Outline each Plasmodium malariae-infected red blood cell.
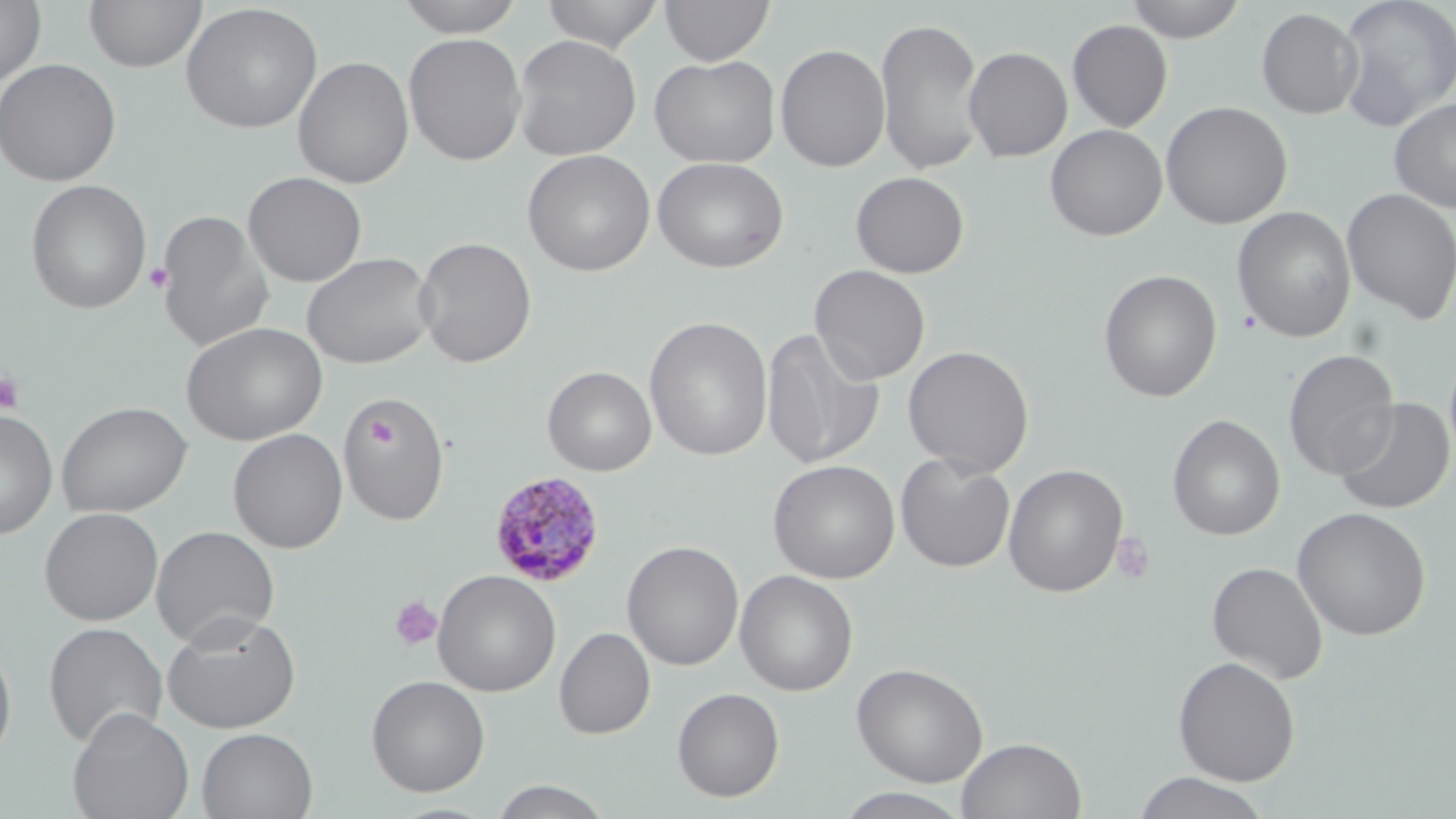

Approximate bounding boxes as (x1, y1, x2, y2) in pixels.
Plasmodium malariae-infected red blood cells: (488, 471, 606, 587).

Summary:
  - Uninfected red blood cell locations: (84, 0, 207, 73), (392, 0, 528, 37), (540, 0, 665, 51), (660, 0, 774, 65), (1125, 0, 1248, 42), (1336, 0, 1456, 131), (0, 1, 47, 88), (180, 3, 323, 133), (1256, 8, 1363, 119), (875, 15, 986, 176), (1067, 20, 1172, 132), (403, 32, 527, 166), (512, 34, 641, 160), (775, 44, 891, 171), (964, 46, 1072, 162), (649, 54, 781, 169), (292, 55, 414, 188), (0, 58, 122, 187), (1389, 98, 1456, 213), (1160, 101, 1293, 229), (1045, 124, 1167, 241), (521, 149, 656, 276), (653, 156, 789, 273), (243, 171, 367, 286), (851, 171, 969, 278), (25, 179, 151, 315), (1341, 188, 1456, 324), (1231, 206, 1357, 343), (154, 209, 274, 352), (414, 236, 537, 367), (302, 252, 436, 369), (809, 264, 931, 384), (1098, 269, 1222, 402), (644, 316, 773, 461), (181, 322, 327, 445), (760, 328, 884, 469), (902, 345, 1034, 477), (1283, 348, 1400, 480), (542, 366, 657, 476), (339, 394, 450, 526), (1333, 398, 1454, 515), (55, 401, 192, 518), (0, 409, 58, 540), (1167, 414, 1285, 540), (228, 428, 347, 553), (895, 453, 1016, 572), (767, 459, 901, 584), (1003, 464, 1128, 597), (39, 507, 163, 625), (1292, 507, 1431, 640), (151, 526, 280, 648), (622, 540, 744, 671), (1206, 561, 1328, 684), (432, 569, 561, 696), (735, 569, 858, 696), (162, 611, 302, 733), (43, 622, 168, 749), (555, 626, 656, 739), (0, 637, 17, 766), (1173, 656, 1301, 785), (852, 662, 989, 787), (366, 675, 490, 796), (672, 687, 784, 801), (66, 707, 195, 819), (197, 727, 318, 819), (957, 736, 1086, 818), (1132, 772, 1271, 819), (490, 779, 613, 818), (835, 788, 972, 818)
  - Platelet locations: (144, 262, 174, 294), (0, 371, 25, 415), (368, 419, 395, 446), (1110, 530, 1156, 585), (390, 596, 443, 651)
  - Slide-level diagnosis: Plasmodium malariae
  - Field of view: one of a larger specimen
  - Magnification: 1000x
  - Modality: light microscopy
  - Stain: May-Grünwald-Giemsa
  - Preparation: thin blood film
  - Image size: 1456×819 pixels